Comment on the morphology of the erythrocytes.
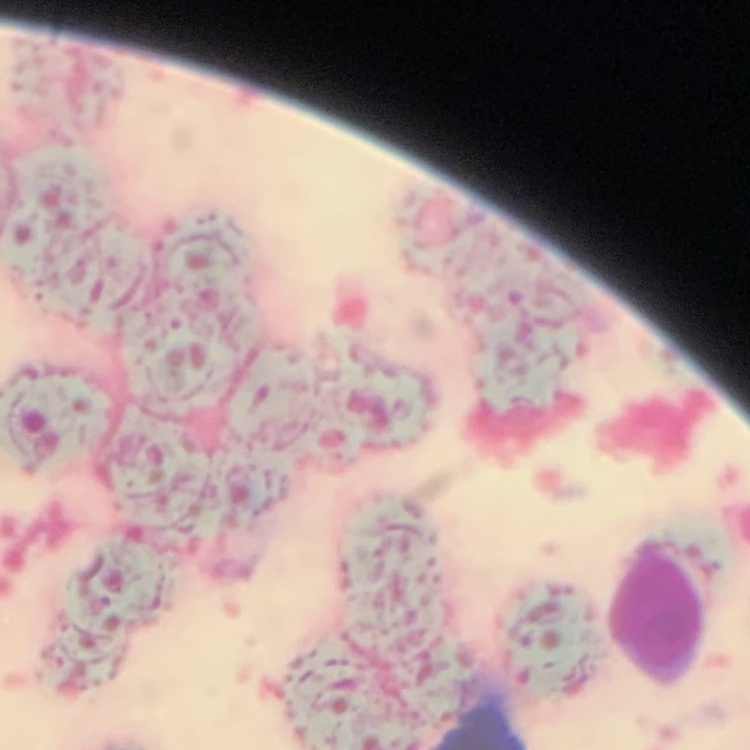

They show rouleaux formation.

Square crop of a larger photomicrograph. Field's or Giemsa stain. Thin peripheral smear.